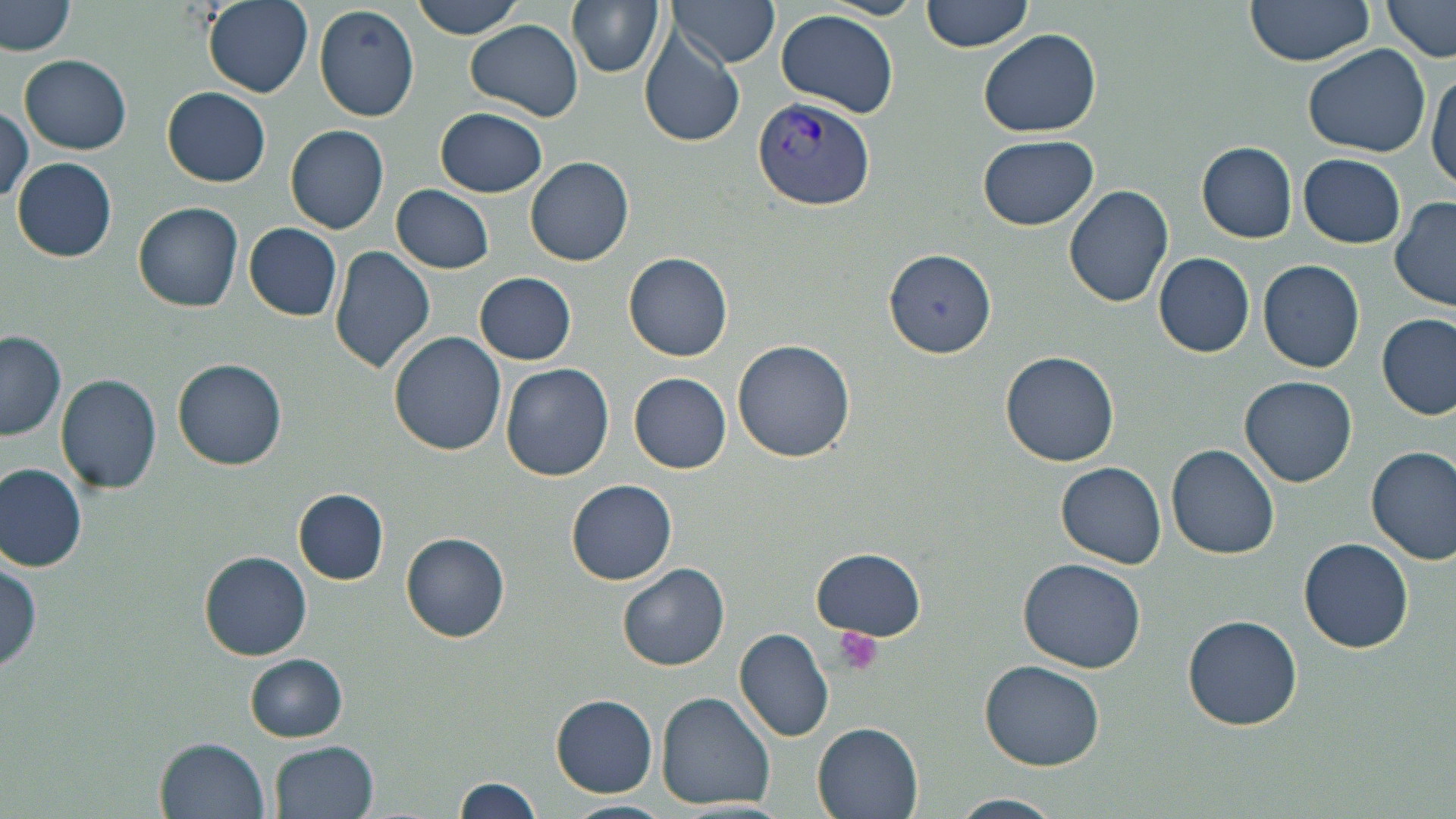

Summary:
  - Coordinate format: approximate bounding boxes as [x1, y1, x2, y2] in pixels
  - Platelet locations: [833, 625, 883, 676]
  - Uninfected red blood cell locations: [201, 0, 315, 98], [407, 0, 527, 39], [566, 0, 665, 77], [668, 0, 779, 68], [922, 0, 1033, 53], [1243, 0, 1377, 66], [1381, 0, 1456, 62], [2, 1, 76, 56], [313, 5, 420, 121], [654, 6, 763, 112], [777, 9, 900, 119], [466, 19, 583, 120], [979, 28, 1101, 137], [639, 30, 745, 148], [1304, 44, 1429, 157], [20, 55, 132, 154], [1428, 69, 1455, 192], [164, 87, 271, 186], [0, 107, 33, 204], [435, 108, 547, 198], [286, 125, 388, 233], [977, 134, 1099, 230], [1197, 142, 1297, 241], [1299, 153, 1405, 248], [526, 156, 634, 266], [12, 158, 116, 262], [390, 185, 495, 273], [1064, 185, 1174, 310], [1390, 198, 1456, 311], [133, 202, 244, 312], [244, 224, 344, 320], [330, 247, 436, 375], [883, 250, 996, 356], [625, 251, 733, 361], [1153, 253, 1256, 358], [1258, 258, 1365, 371], [475, 272, 577, 365], [1378, 313, 1454, 419], [0, 332, 66, 440], [388, 332, 506, 457], [733, 339, 854, 462], [999, 352, 1119, 467], [172, 359, 286, 469], [500, 363, 614, 479], [56, 372, 162, 496], [629, 372, 731, 473], [1240, 375, 1358, 488], [1166, 443, 1280, 560], [1367, 445, 1456, 565], [1056, 462, 1167, 568], [0, 465, 87, 571], [567, 479, 677, 585], [294, 489, 388, 584], [401, 533, 510, 642], [1300, 538, 1413, 654], [812, 548, 925, 641], [200, 550, 312, 659], [1, 555, 44, 674], [1018, 558, 1149, 674], [620, 565, 730, 671], [1182, 614, 1303, 731], [735, 627, 834, 742], [245, 654, 348, 742], [981, 659, 1106, 770], [657, 692, 775, 808], [553, 696, 657, 796], [813, 722, 925, 819], [157, 738, 269, 817], [273, 740, 381, 819], [453, 777, 546, 818], [946, 794, 1067, 819], [559, 799, 673, 819]
  - Plasmodium vivax-infected red blood cell locations: [752, 97, 876, 207]
  - Slide-level diagnosis: Plasmodium vivax
  - Modality: optical microscopy
  - Field of view: one of a larger specimen
  - Preparation: thin blood smear
  - Image size: 1456×819 pixels
  - Magnification: 1000x
  - Stain: May-Grünwald-Giemsa